Identify the cell.
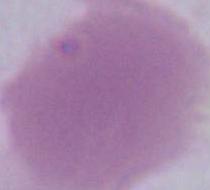

This is an erythrocyte.

Captured at 1000x magnification. Photomicrograph.